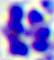 Micrograph. A white blood cell is seen. 400x magnification.